Point out each malaria parasite and each leukocyte.
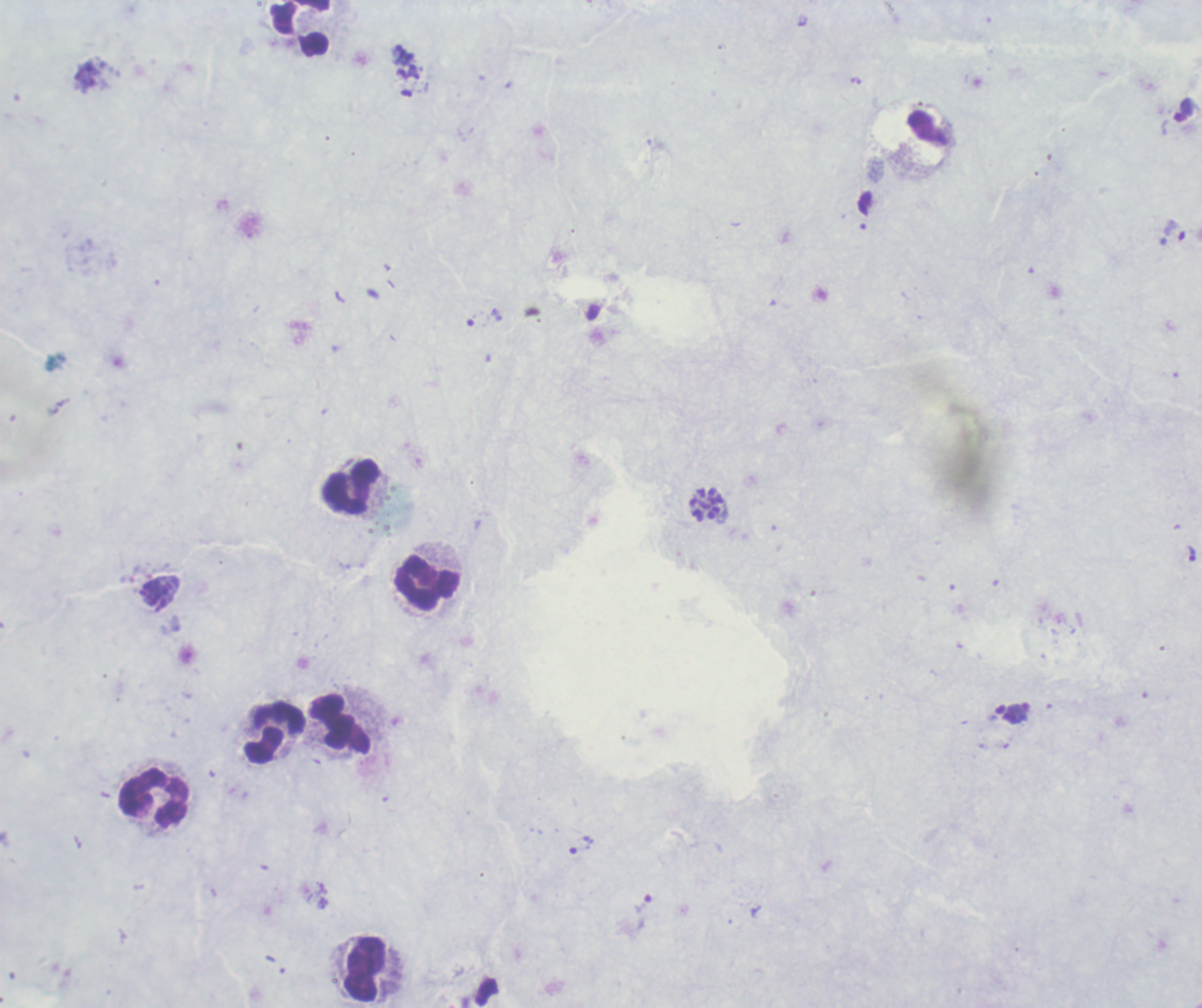
Approximate centers as [x, y] in pixels.
Trophozoites: [581, 844], [642, 903].
Schizonts: [406, 61], [707, 505].
No gametocyte forms observed.
Leukocytes: [301, 29], [352, 487], [427, 584], [341, 725], [275, 733], [154, 799], [365, 969].

Summary:
  - Magnification: 100x
  - Stain: Romanowsky
  - Context: previously used in an actual diagnosis
  - Field of view: one from this slide
  - Preparation: thick blood smear
  - Image size: 1202×1008 pixels
  - Background quality: unsatisfactory